Classify this cell by malaria status.
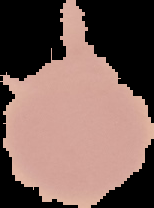
Uninfected.

The area outside the segmented cell region is set to black. From a thin blood smear. Image is 154×208 pixels.